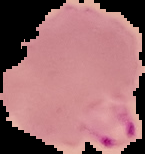
result: Plasmodium parasites identified
preparation: thin blood smear
image_size: 145×154 pixels
image_type: cell region segmented out of the field of view; surrounding area masked to black